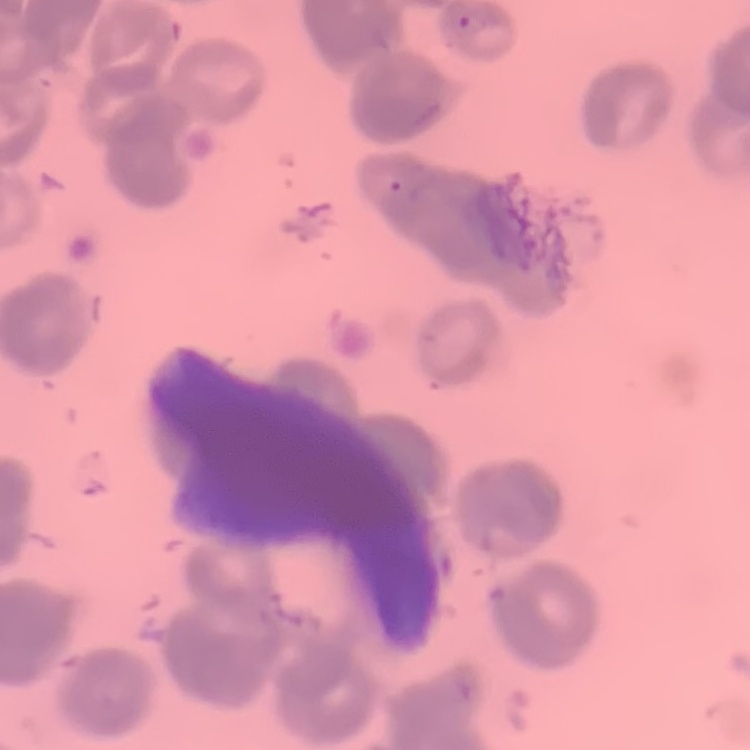
Summary:
  - Red blood cell morphology: rouleaux formation
  - Preparation: thin peripheral smear
  - Stain: Field's or Giemsa
  - Image type: one tile cut from a larger photomicrograph